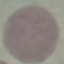
Result: no malaria parasites seen. Photographed with a smartphone camera at the microscope eyepiece. Automatically extracted cell patch, resized to 64 × 64 pixels. Giemsa stain. Thin blood smear.